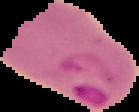

Summary:
  - Image type: segmented cell region on a black background
  - Malaria status: parasitized
  - Image size: 139×112 pixels
  - Preparation: thin blood smear